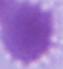

Summary:
  - Modality: photomicrograph
  - Magnification: 1000x
  - Identification: red blood cell